Assess the background quality.
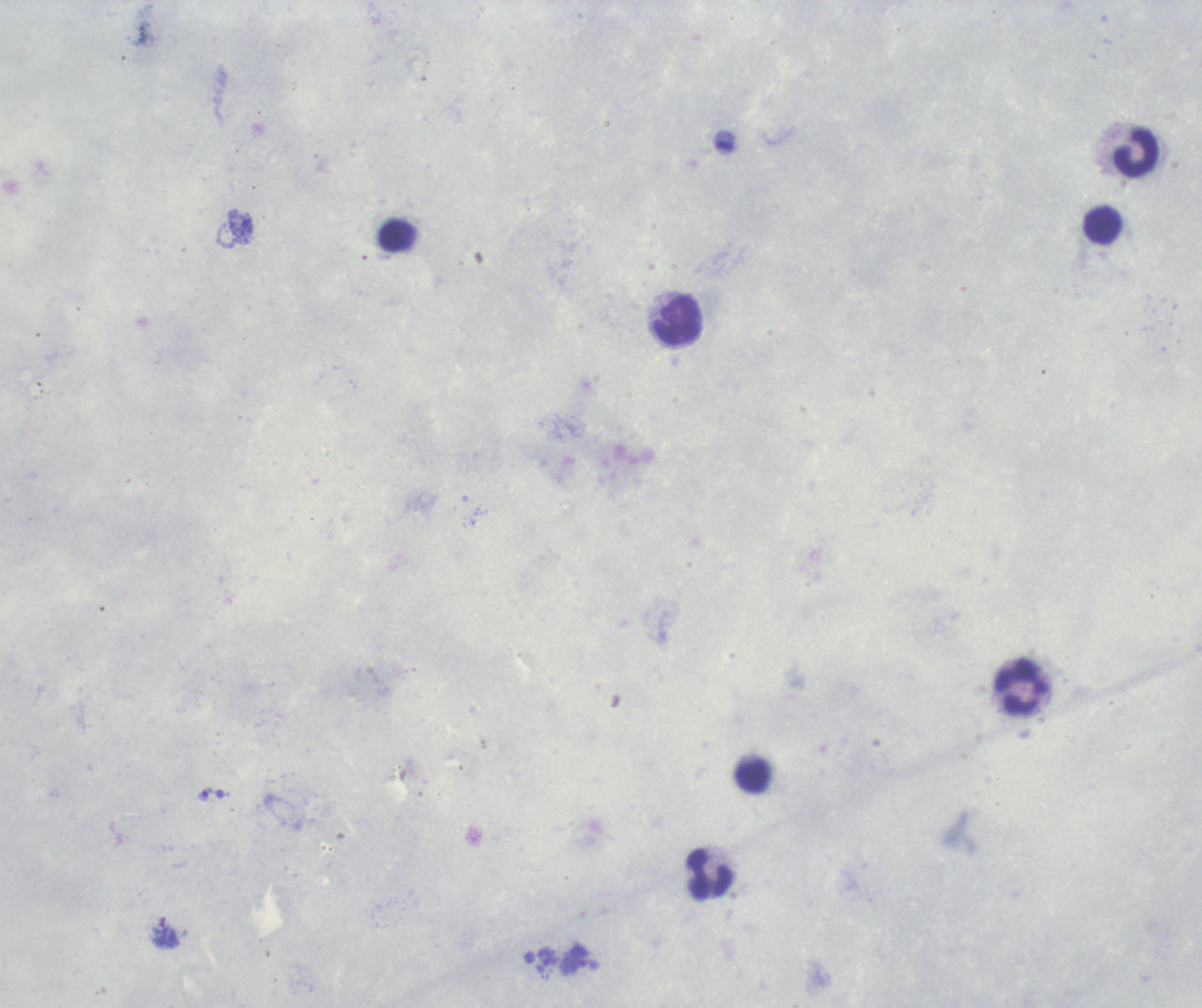
It is poor.

Approximate centers as [x, y] in pixels. Leukocyte locations: [1136, 153], [1103, 226], [677, 321], [1022, 687], [709, 875]. Trophozoite locations: [205, 794]. Image is 1202×1008 pixels. Romanowsky stain. Thick smear of blood. Captured at 100x magnification. One field from this slide. Result: Plasmodium parasites identified. Previously used in a real diagnosis.